Report the malaria status of this cell.
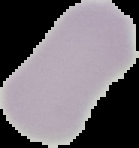
Uninfected.

Summary:
  - Preparation: thin blood smear
  - Image type: cell region segmented out of the field of view; surrounding area masked to black
  - Image size: 139×148 pixels